Locate Plasmodium parasites and leukocytes.
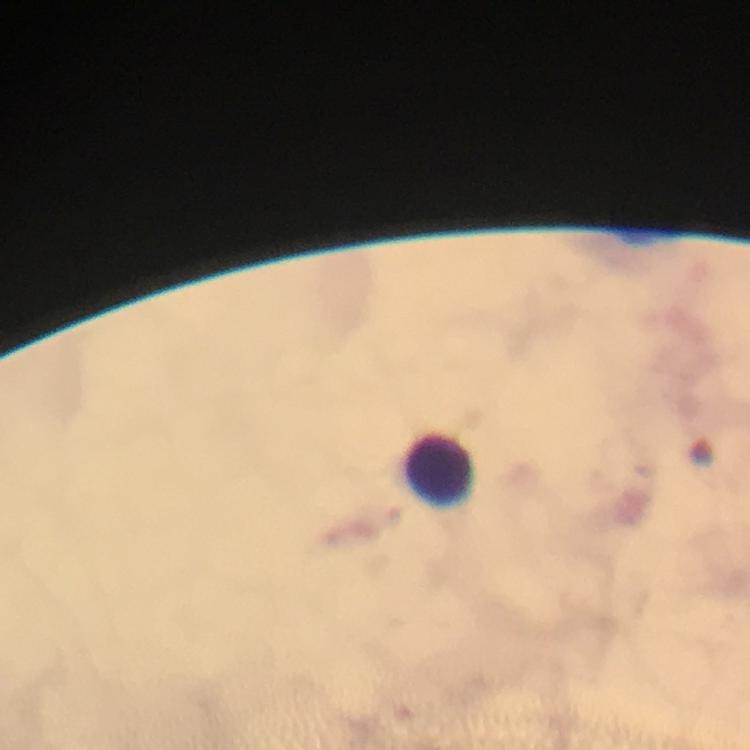

No Plasmodium parasites seen.
Approximate centers as [x, y] in pixels.
Leukocytes: [438, 467].

immersion_oil: used
stain: Giemsa
cropped_from: one field of view
context: from a diagnostic examination for malaria
image_size: 750×750 pixels
preparation: thick smear
capture: smartphone camera through the microscope
magnification: 100x